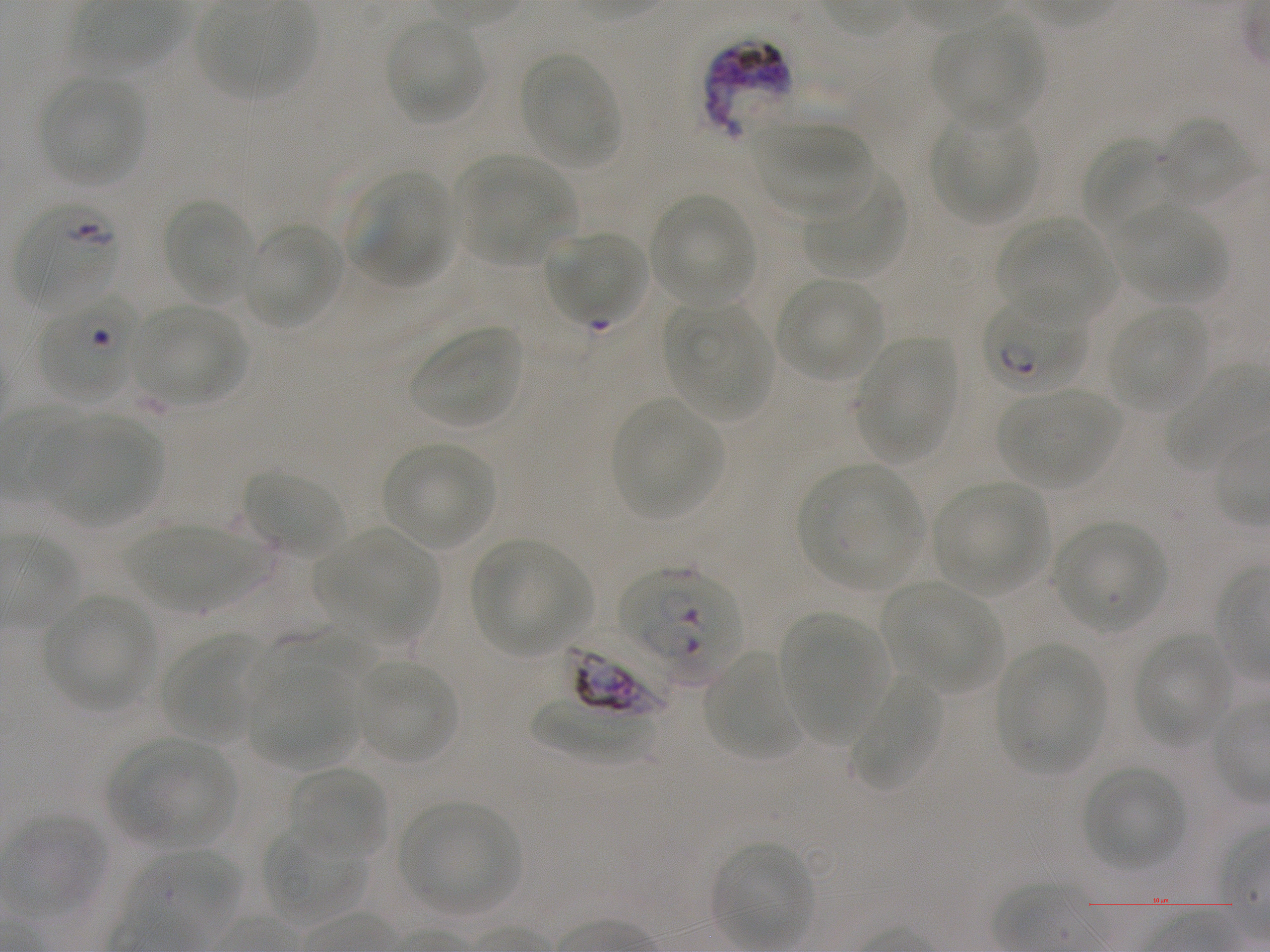
Approximate bounding boxes as {x1, y1, x2, y2} in pixels. Not every red blood cell is marked. A life-cycle stage — or a range of stages, where the recorded stages span more than one — follows each staged infected red blood cell. Locations of red blood cells of indeterminate infection status: {705, 39, 793, 138}, {566, 633, 678, 718}. Locations of infected red blood cells: {15, 206, 120, 313}; {40, 294, 142, 400}; {984, 295, 1091, 392} early ring to early trophozoite; {620, 567, 743, 682}. Locations of uninfected red blood cells: {936, 17, 1044, 127}, {385, 19, 485, 124}, {518, 52, 622, 170}, {38, 76, 145, 186}, {931, 114, 1038, 225}, {1155, 116, 1252, 206}, {753, 124, 873, 216}, {1081, 139, 1174, 236}, {457, 156, 574, 264}, {350, 172, 454, 287}, {804, 174, 906, 279}, {648, 194, 758, 308}, {163, 198, 255, 304}, {1118, 205, 1227, 304}, {998, 216, 1114, 323}, {244, 223, 344, 329}, {550, 230, 648, 325}, {775, 278, 884, 382}, {666, 302, 770, 421}, {134, 306, 246, 406}, {1109, 306, 1208, 412}, {408, 325, 523, 429}, {855, 338, 958, 460}, {1163, 365, 1267, 473}, {1001, 388, 1122, 488}, {612, 399, 722, 519}, {37, 415, 164, 525}, {383, 441, 497, 549}, {801, 464, 923, 589}, {242, 470, 345, 556}, {934, 483, 1049, 595}, {1054, 521, 1168, 632}, {124, 526, 264, 612}, {320, 528, 440, 641}, {471, 540, 591, 654}, {883, 582, 1000, 690}, {43, 594, 159, 711}, {780, 615, 885, 744}, {247, 625, 377, 696}, {164, 636, 261, 741}, {1134, 636, 1233, 746}, {997, 646, 1106, 774}, {702, 650, 803, 763}, {355, 659, 458, 765}, {249, 671, 358, 767}, {850, 676, 944, 788}, {530, 699, 656, 765}, {112, 738, 234, 847}, {290, 765, 387, 864}, {1084, 766, 1185, 870}, {399, 801, 520, 915}, {6, 817, 109, 916}, {262, 826, 367, 923}, {713, 842, 814, 948}, {131, 849, 241, 938}. 100x oil-immersion objective, numerical aperture 1.25. Image is 1270×952 pixels. One field from this slide. Donor blood group A+. Giemsa-stained preparation. P. falciparum strain NF54 in static in-vitro culture. Thin blood smear.